Give the position of every leukocyte visible.
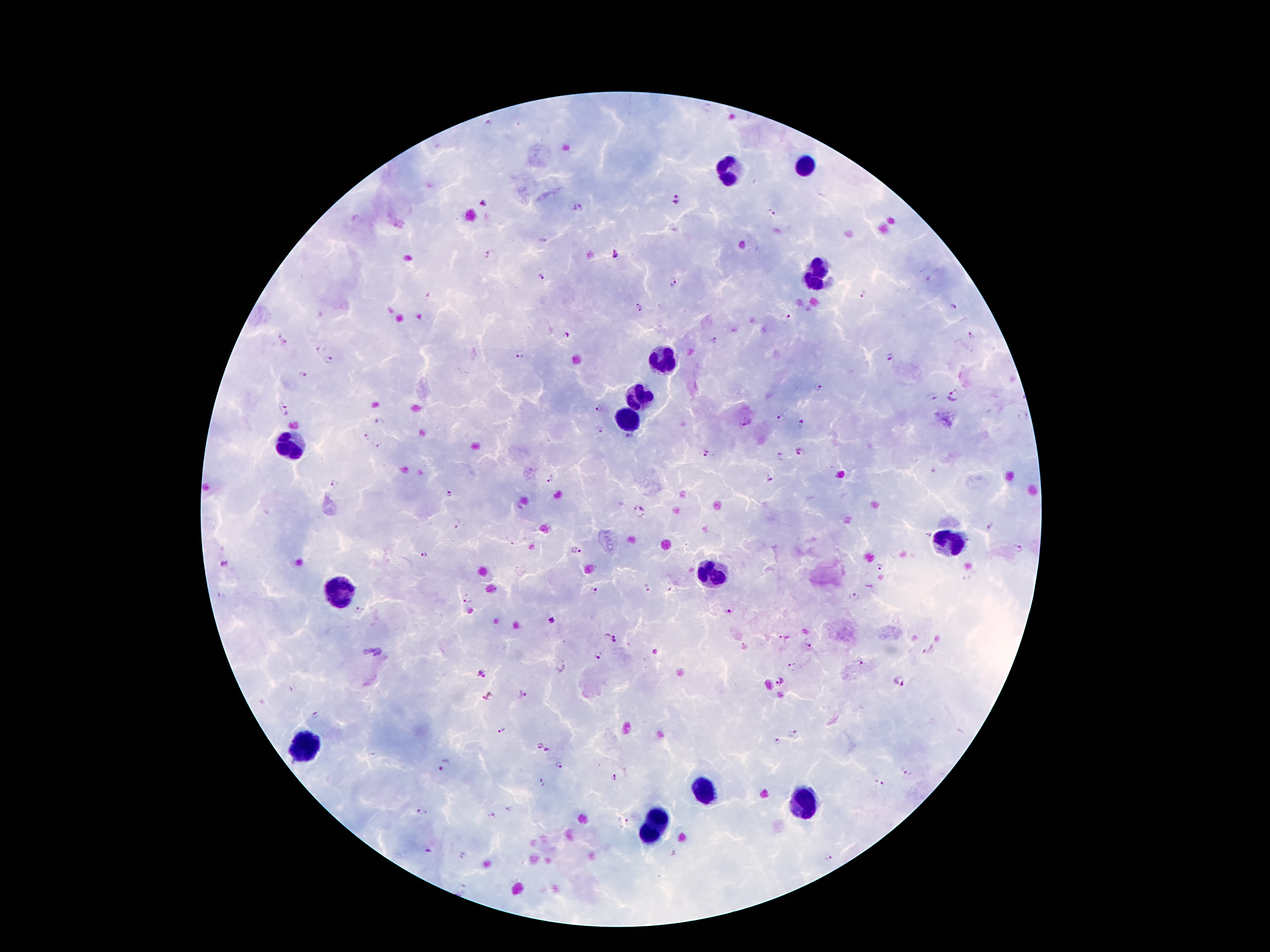
Approximate centers as (x, y) in pixels.
Leukocytes: (804, 165), (729, 171), (817, 276), (660, 357), (640, 397), (627, 417), (293, 441), (946, 545), (713, 572), (338, 593), (304, 746), (702, 791), (804, 802), (658, 815), (647, 834).

Plasmodium parasite locations = (673, 200), (486, 204), (579, 208), (772, 214), (614, 253), (488, 255), (541, 277), (672, 282), (863, 293), (953, 307), (639, 308), (786, 319), (566, 334), (971, 336), (712, 340), (284, 342), (521, 353), (889, 356), (329, 360), (301, 376), (819, 387), (954, 395), (931, 397), (599, 408), (284, 410), (780, 418), (380, 422), (747, 422), (801, 424), (599, 429), (378, 444), (800, 451), (706, 452), (781, 456), (769, 479), (551, 481), (335, 484), (450, 495), (639, 512), (457, 523), (989, 526), (925, 535), (1018, 549), (576, 551), (424, 555), (224, 565), (882, 567), (648, 588), (595, 590), (856, 597), (467, 598), (359, 611), (729, 612), (471, 613), (553, 619), (616, 638), (784, 638), (808, 645), (371, 652), (655, 653), (599, 655), (860, 663), (561, 667), (792, 668), (479, 673), (901, 683), (782, 684), (521, 694), (488, 697), (314, 717), (502, 731), (795, 734), (776, 741), (538, 744), (546, 750), (445, 764), (560, 765), (906, 773), (612, 776), (542, 783), (877, 783), (511, 810), (421, 812), (493, 817), (623, 823), (428, 850), (828, 857)
patient malaria status = positive for Plasmodium falciparum
preparation = thick blood film
magnification = 100x
field of view = one from this slide
image size = 1270×952 pixels
stain = Giemsa
capture = smartphone camera through the microscope eyepiece